Locate and identify every blood parasite.
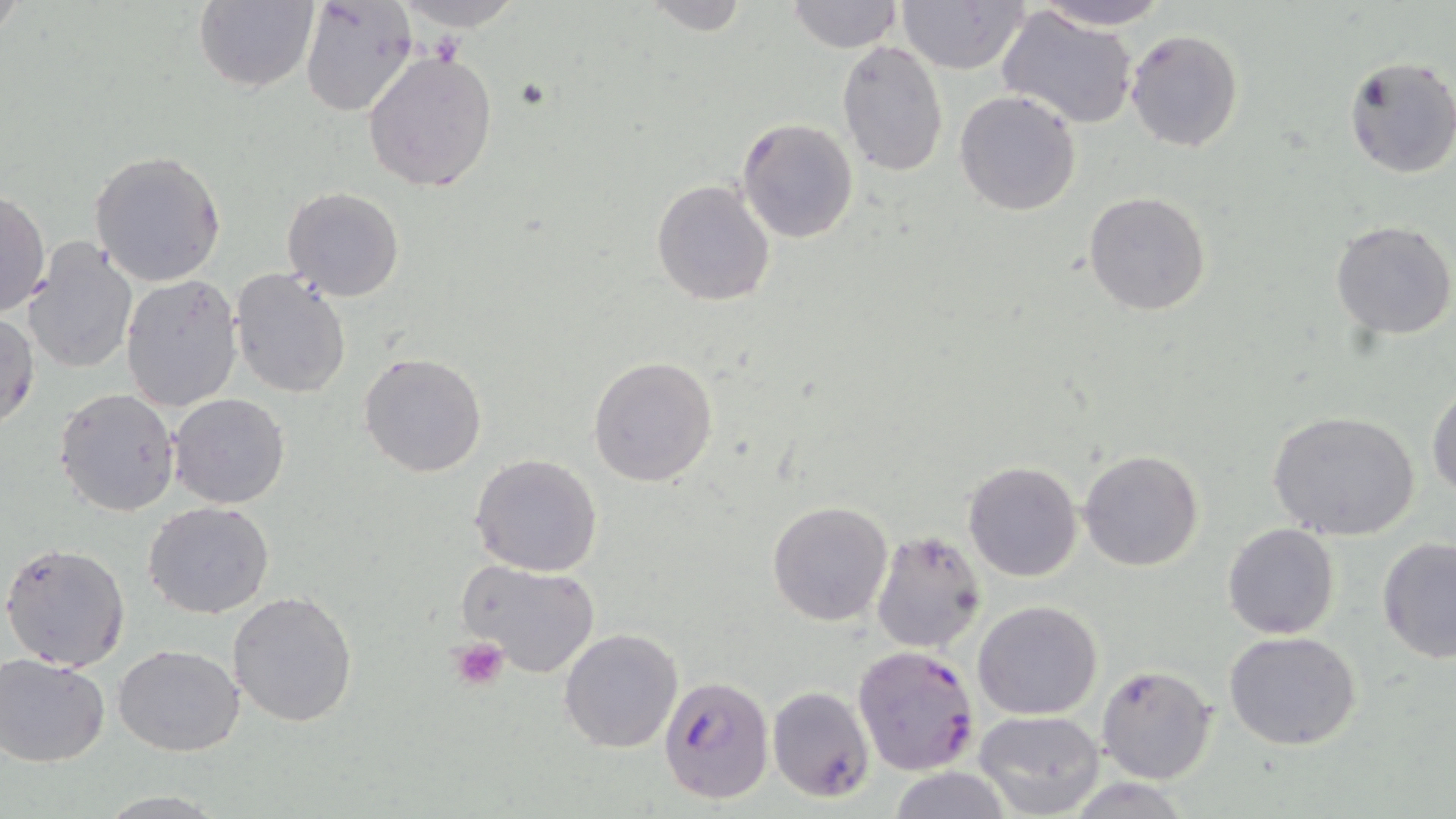
Approximate bounding boxes as [x1, y1, x2, y2] in pixels.
Plasmodium falciparum-infected red blood cells: [852, 645, 980, 777], [659, 677, 773, 805], [767, 686, 875, 802].
No Plasmodium ovale, Plasmodium malariae, Plasmodium vivax, Babesia divergens, or Trypanosoma brucei observed.

Platelet locations: [447, 636, 511, 690]. Uninfected red blood cell locations: [193, 0, 319, 94], [641, 0, 749, 36], [787, 0, 901, 53], [1027, 0, 1174, 30], [298, 1, 419, 120], [388, 1, 528, 32], [897, 2, 1028, 74], [996, 8, 1139, 129], [1124, 28, 1246, 153], [837, 39, 950, 177], [362, 51, 498, 192], [1343, 56, 1456, 179], [954, 89, 1083, 216], [736, 118, 860, 245], [89, 149, 227, 286], [650, 178, 777, 307], [282, 186, 405, 302], [1, 190, 49, 321], [1084, 191, 1213, 316], [1331, 219, 1456, 338], [25, 239, 137, 374], [230, 267, 353, 400], [120, 274, 242, 414], [0, 309, 41, 431], [358, 353, 487, 478], [587, 355, 717, 487], [1427, 384, 1456, 497], [54, 387, 180, 515], [169, 393, 291, 509], [1268, 410, 1422, 542], [1079, 449, 1204, 571], [469, 454, 602, 576], [964, 460, 1084, 583], [767, 500, 895, 627], [143, 501, 275, 620], [1222, 523, 1340, 639], [869, 529, 988, 653], [1376, 536, 1456, 665], [1, 540, 132, 671], [457, 561, 601, 680], [228, 590, 360, 727], [973, 600, 1102, 720], [559, 628, 683, 753], [1225, 632, 1362, 750], [113, 643, 244, 755], [1, 652, 112, 766], [1094, 664, 1218, 785], [975, 710, 1107, 819], [887, 767, 1014, 819]. Slide-level diagnosis: Plasmodium falciparum. 1000x magnification. Image is 1456×819 pixels. Thin blood smear. May-Grünwald-Giemsa-stained preparation. Optical microscopy. One field of a larger specimen.